Name the blood parasite species.
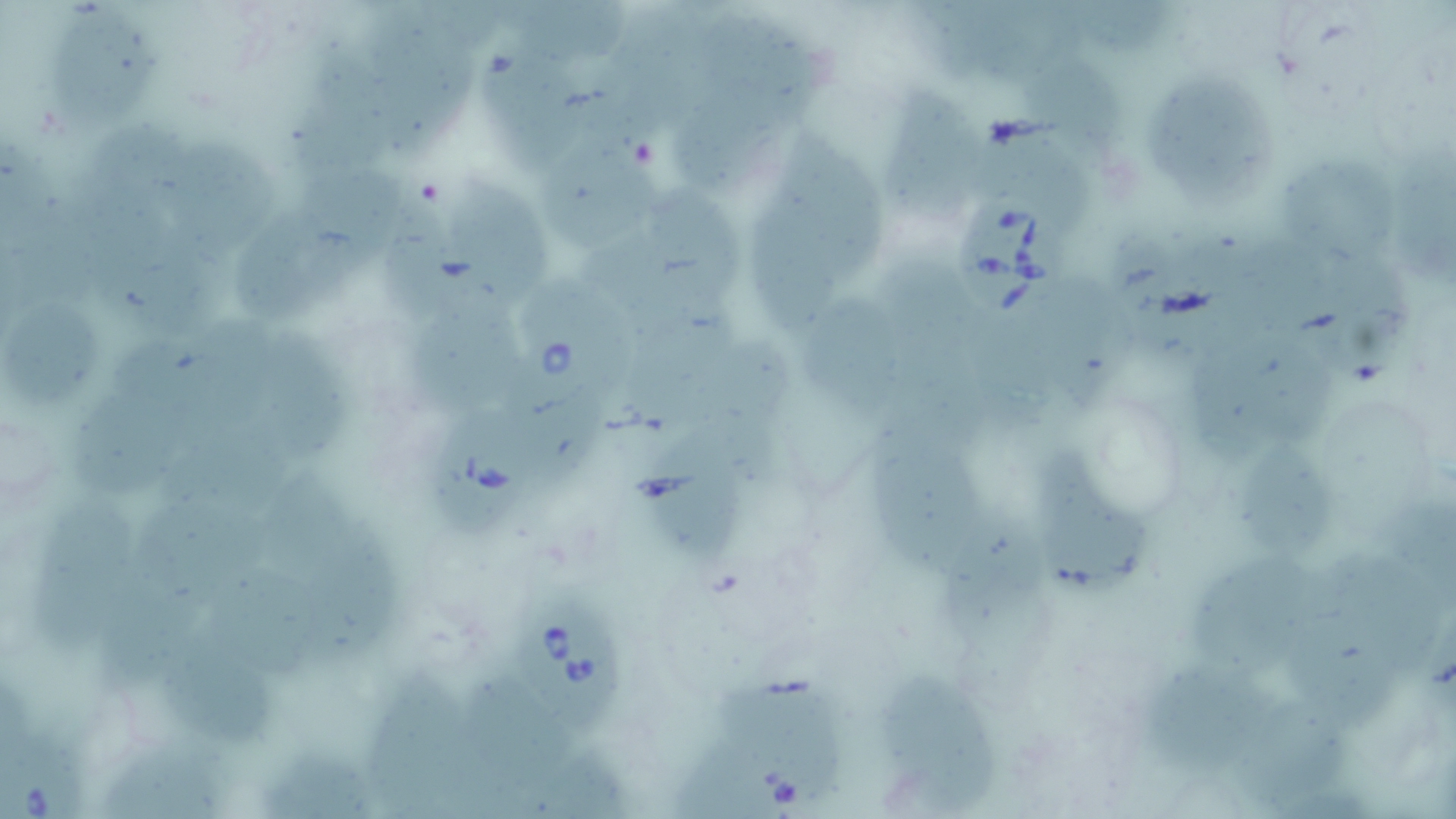
Babesia divergens.

Approximate bounding boxes as [x1, y1, x2, y2] in pixels. Uninfected red blood cell locations: [503, 0, 646, 65], [377, 3, 483, 166], [952, 3, 1090, 101], [55, 13, 176, 140], [704, 13, 826, 113], [607, 17, 721, 140], [491, 49, 587, 174], [307, 63, 389, 203], [1042, 66, 1122, 174], [905, 88, 988, 223], [1168, 90, 1282, 207], [684, 104, 800, 198], [792, 112, 897, 275], [531, 133, 661, 243], [102, 135, 209, 225], [1396, 137, 1456, 289], [1003, 141, 1101, 219], [177, 148, 286, 255], [1278, 161, 1405, 257], [748, 179, 814, 330], [666, 180, 748, 300], [323, 181, 408, 281], [468, 188, 556, 308], [398, 212, 467, 333], [247, 214, 342, 326], [582, 227, 715, 345], [1204, 237, 1323, 325], [105, 239, 235, 334], [1127, 244, 1211, 359], [1334, 266, 1413, 389], [1047, 290, 1133, 406], [814, 292, 901, 399], [1, 297, 107, 422], [417, 316, 523, 408], [184, 318, 280, 444], [1231, 330, 1346, 452], [263, 337, 371, 475], [674, 342, 790, 435], [71, 385, 189, 503], [543, 391, 613, 497], [875, 401, 973, 557], [173, 440, 298, 519], [661, 450, 752, 573], [1038, 450, 1149, 605], [1247, 454, 1341, 560], [268, 464, 363, 570], [39, 490, 146, 648], [1373, 494, 1456, 608], [142, 497, 275, 578], [940, 510, 1035, 636], [327, 546, 405, 664], [1180, 553, 1306, 666], [1339, 553, 1451, 683], [218, 565, 353, 680], [110, 568, 214, 703], [1283, 570, 1408, 735], [172, 628, 283, 741], [1142, 650, 1262, 769], [379, 671, 468, 818], [457, 671, 560, 817], [879, 671, 996, 806], [731, 676, 849, 777], [1237, 691, 1357, 804], [99, 735, 233, 819], [271, 738, 389, 814], [676, 738, 774, 819], [544, 742, 639, 813]. Babesia divergens-infected red blood cell locations: [956, 192, 1068, 318], [515, 275, 637, 410], [434, 408, 538, 534], [521, 596, 627, 742], [1, 718, 103, 819]. Thin blood film. Captured at 1000x magnification. Light microscopy. Image is 1456×819 pixels. Single field of view. May-Grünwald-Giemsa-stained preparation.